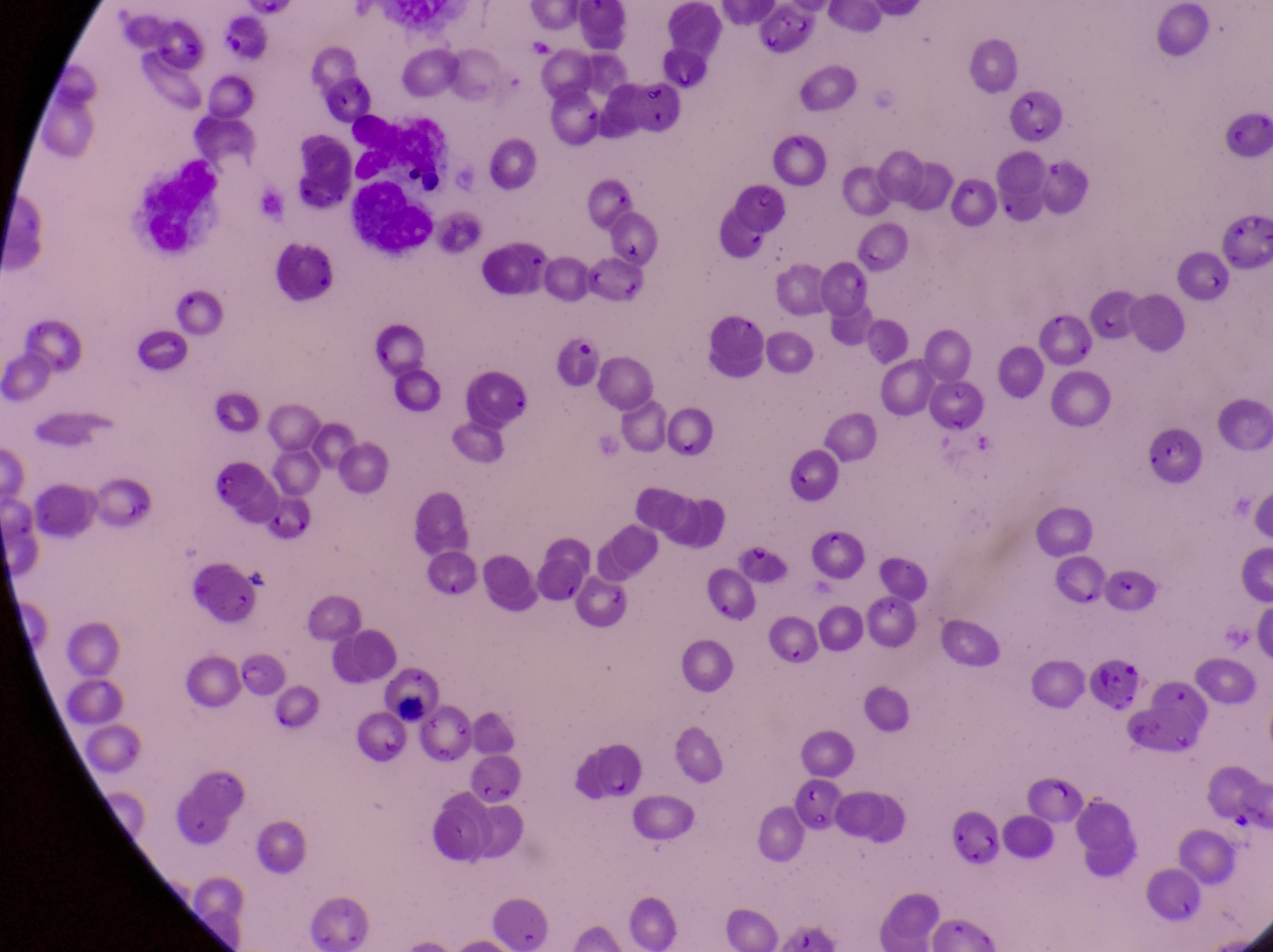

{
  "capture": "smartphone photograph through the eyepiece of an Olympus CX-23 microscope",
  "image_size": "1273×952 pixels",
  "preparation": "thin blood film",
  "magnification": "1000x",
  "parasitised_red_blood_cell_locations": "approximate bounding boxes as {left, top, right, bottom} in pixels: {460, 354, 530, 428}, {230, 649, 282, 697}",
  "country": "Uganda",
  "field_of_view": "single"
}